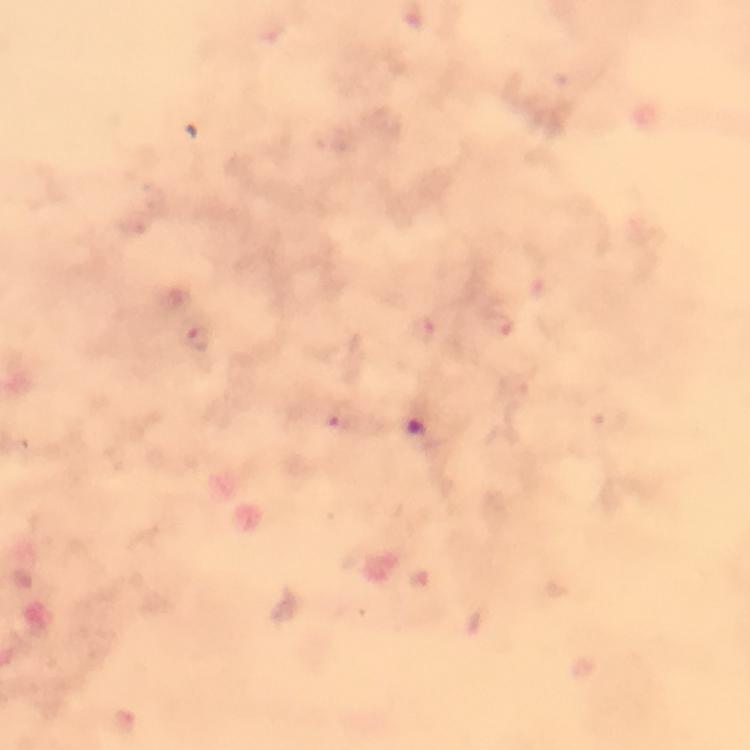
Approximate centers as {x, y} in pixels.
Summary:
  - Plasmodium parasite locations: {349, 417}
  - Immersion oil: applied
  - Preparation: thick blood smear
  - Image size: 750×750 pixels
  - Context: from a malaria diagnostic workup
  - Cropped from: a single field of view
  - Stain: Giemsa
  - Magnification: 100x
  - Capture: smartphone camera through the microscope